Outline every malaria parasite, every leukocyte, and every artifact (stain precipitate or debris).
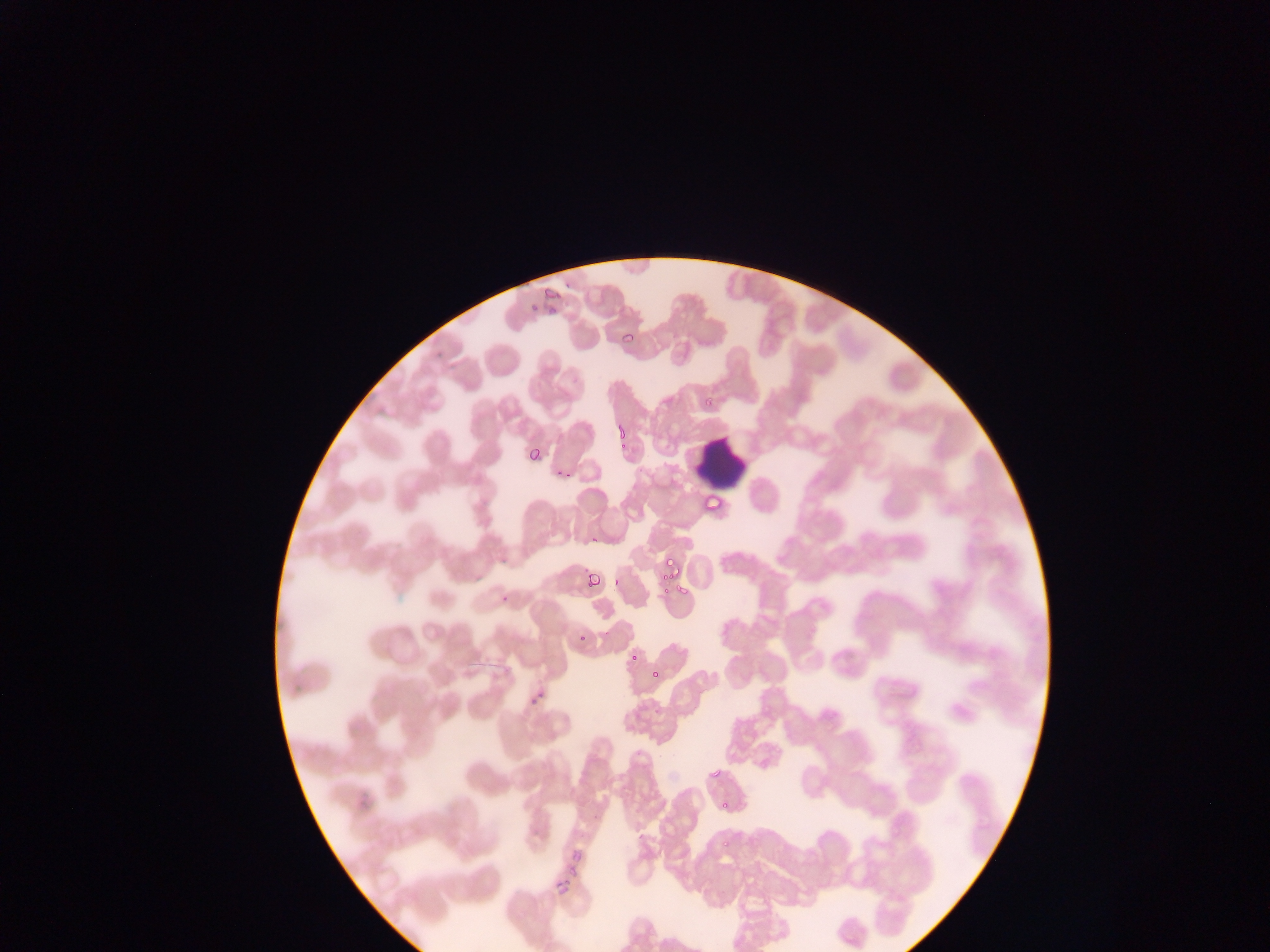
Approximate bounding boxes as (left, top, right, bottom) in pixels.
Malaria parasites: (563, 279, 571, 288), (540, 284, 560, 306), (528, 299, 538, 312), (546, 304, 560, 315), (620, 329, 635, 345), (700, 393, 715, 406), (615, 422, 629, 437), (615, 441, 628, 453), (525, 443, 542, 463), (555, 467, 566, 478), (562, 470, 572, 482), (701, 491, 721, 513), (588, 532, 600, 546), (661, 555, 678, 574), (581, 568, 595, 576), (584, 572, 601, 589), (610, 576, 621, 587), (658, 577, 677, 597), (500, 583, 515, 604), (677, 583, 690, 597), (660, 584, 672, 597), (656, 586, 668, 596), (577, 631, 589, 643), (629, 652, 640, 665), (647, 664, 663, 682), (526, 694, 545, 711), (761, 699, 771, 711), (653, 707, 661, 715), (770, 745, 783, 757), (708, 765, 725, 781), (718, 797, 731, 812), (592, 814, 598, 822), (722, 836, 733, 849), (563, 846, 589, 873), (553, 857, 583, 890), (552, 871, 575, 895) | approximate (x, y) pixel centers of objects too small to bound: (607, 632).
Leukocytes: (695, 441, 748, 485).

Summary:
  - Image size: 1270×952 pixels
  - Field of view: single
  - Preparation: thin blood film
  - Country: Ghana
  - Capture: mobile-phone photograph through a microscope